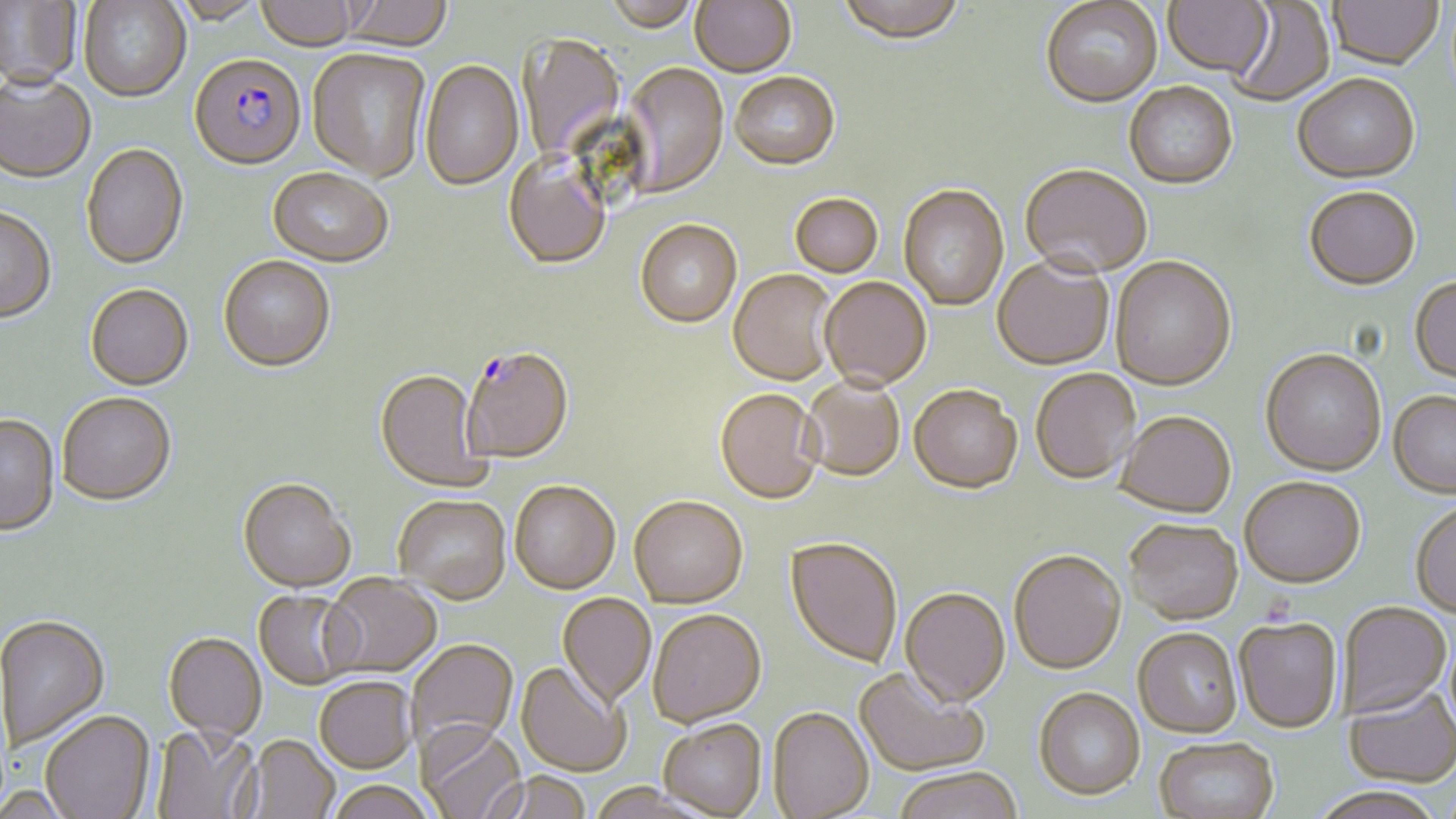
Approximate bounding boxes as (x1,y1)-(x2,y2) corner pairs in pixels. Plasmodium falciparum-infected red blood cell locations: (190,52)-(306,168), (462,344)-(573,462). Uninfected red blood cell locations: (2,0)-(81,87), (167,0)-(267,24), (256,0)-(363,49), (339,0)-(455,48), (689,0)-(797,77), (835,0)-(968,47), (1327,0)-(1445,70), (79,1)-(190,101), (601,1)-(699,32), (1040,1)-(1163,109), (1163,1)-(1274,78), (1226,2)-(1335,107), (518,33)-(627,163), (307,47)-(431,182), (420,59)-(525,190), (622,63)-(728,197), (0,72)-(96,182), (729,72)-(841,171), (1292,75)-(1420,184), (1125,82)-(1238,190), (81,142)-(188,268), (503,153)-(611,269), (1020,164)-(1151,278), (267,165)-(394,265), (898,185)-(1008,311), (1304,187)-(1421,291), (790,193)-(884,278), (0,206)-(57,321), (635,219)-(743,328), (218,254)-(336,370), (993,256)-(1114,370), (1110,256)-(1236,390), (728,269)-(837,385), (820,276)-(932,391), (1410,277)-(1456,384), (85,282)-(193,389), (1260,348)-(1386,475), (375,368)-(490,491), (1030,368)-(1140,484), (800,377)-(905,482), (909,385)-(1022,493), (715,387)-(823,504), (57,391)-(176,504), (1388,391)-(1456,499), (1115,410)-(1236,517), (0,415)-(60,536), (1240,475)-(1366,587), (238,476)-(356,591), (510,479)-(620,593), (393,494)-(511,603), (628,494)-(748,607), (1410,501)-(1456,619), (1124,518)-(1242,624), (785,536)-(903,667), (1008,549)-(1126,674), (321,572)-(442,677), (900,586)-(1010,706), (253,590)-(360,689), (557,593)-(656,706), (1338,602)-(1451,718), (647,608)-(766,726), (1,614)-(110,749), (1234,616)-(1342,733), (1133,627)-(1243,737), (163,632)-(266,740), (406,638)-(518,753), (516,660)-(629,776), (854,666)-(989,776), (314,676)-(416,772), (1344,685)-(1456,788), (1033,687)-(1146,800), (768,706)-(874,818), (41,709)-(155,818), (658,718)-(767,817), (418,721)-(526,819), (152,725)-(260,819), (243,734)-(340,819), (1154,736)-(1279,819), (892,766)-(1024,819), (482,770)-(593,819), (327,780)-(435,819), (1307,786)-(1447,818). Slide-level diagnosis: Plasmodium falciparum. May-Grünwald-Giemsa stain. Thin blood smear. Image is 1456×819 pixels. One field of a larger specimen. Captured at 1000x magnification. Light microscopy.